Classify this cell by malaria status.
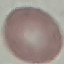
Uninfected.

{
  "image_type": "automatically extracted cell patch, resized to 64 × 64 pixels",
  "preparation": "thin smear",
  "stain": "Giemsa",
  "capture": "smartphone through the microscope eyepiece"
}